Name the blood parasite species.
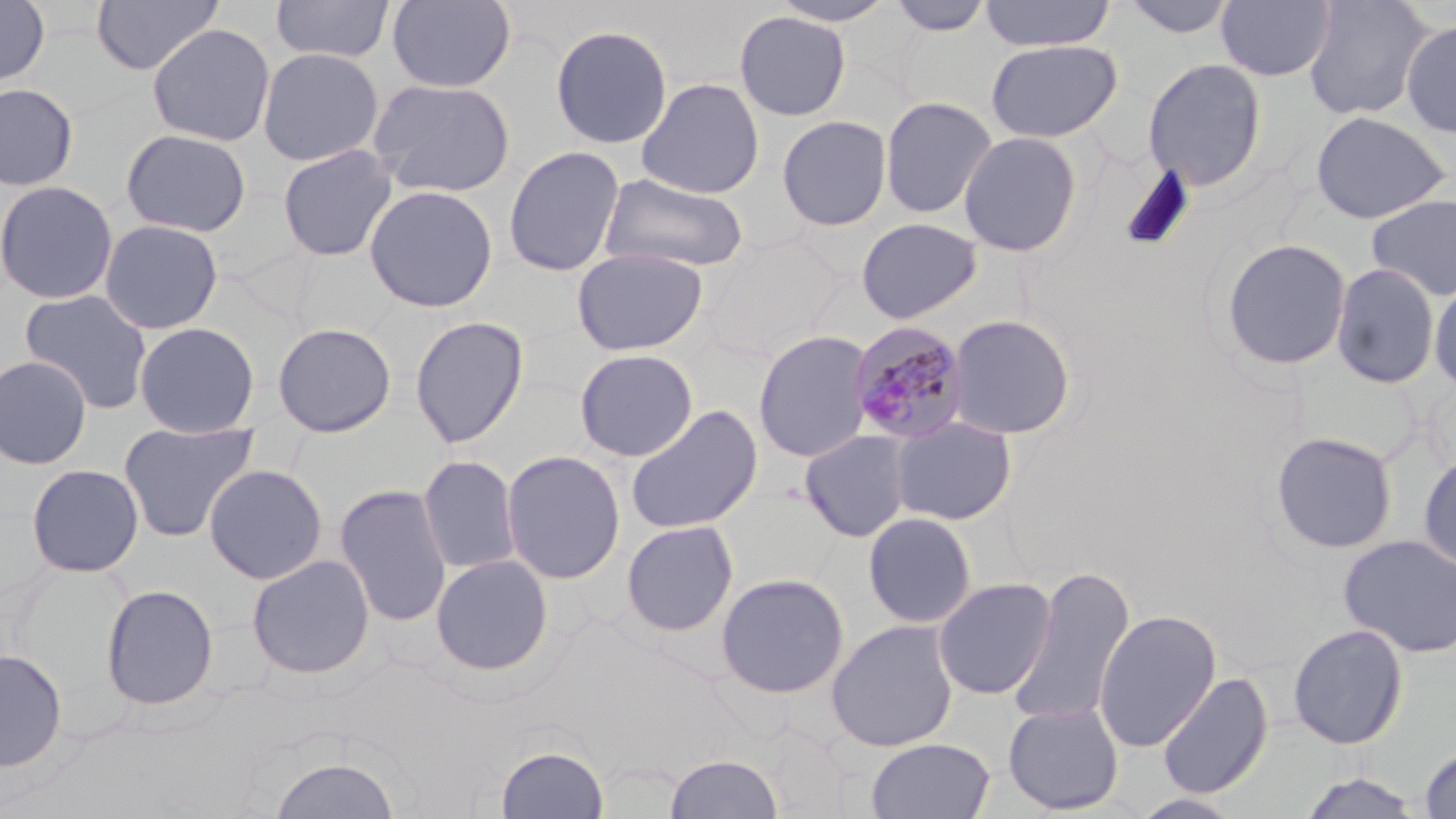
Plasmodium malariae.

Approximate bounding boxes as named x1/y1/x2/y2 corners in pixels. Uninfected red blood cell locations: (x1=0, y1=0, x2=50, y2=88), (x1=90, y1=0, x2=222, y2=76), (x1=270, y1=0, x2=396, y2=64), (x1=387, y1=0, x2=516, y2=93), (x1=769, y1=0, x2=899, y2=26), (x1=886, y1=0, x2=995, y2=36), (x1=980, y1=0, x2=1115, y2=52), (x1=1119, y1=0, x2=1239, y2=39), (x1=1216, y1=0, x2=1336, y2=81), (x1=1302, y1=0, x2=1433, y2=120), (x1=734, y1=10, x2=851, y2=121), (x1=1400, y1=18, x2=1456, y2=140), (x1=147, y1=22, x2=276, y2=146), (x1=550, y1=24, x2=673, y2=149), (x1=985, y1=39, x2=1123, y2=142), (x1=257, y1=46, x2=385, y2=167), (x1=1141, y1=58, x2=1267, y2=190), (x1=367, y1=77, x2=515, y2=198), (x1=636, y1=77, x2=765, y2=199), (x1=0, y1=82, x2=79, y2=192), (x1=879, y1=96, x2=998, y2=219), (x1=1309, y1=110, x2=1451, y2=224), (x1=777, y1=114, x2=892, y2=231), (x1=120, y1=128, x2=252, y2=237), (x1=958, y1=131, x2=1083, y2=257), (x1=276, y1=144, x2=398, y2=262), (x1=503, y1=145, x2=625, y2=276), (x1=598, y1=172, x2=750, y2=273), (x1=0, y1=179, x2=119, y2=305), (x1=363, y1=184, x2=499, y2=312), (x1=1365, y1=194, x2=1456, y2=302), (x1=856, y1=217, x2=983, y2=325), (x1=99, y1=219, x2=223, y2=334), (x1=703, y1=234, x2=843, y2=358), (x1=1218, y1=238, x2=1353, y2=372), (x1=570, y1=246, x2=709, y2=356), (x1=1330, y1=262, x2=1441, y2=389), (x1=1429, y1=279, x2=1456, y2=396), (x1=19, y1=289, x2=154, y2=415), (x1=946, y1=314, x2=1077, y2=440), (x1=409, y1=315, x2=529, y2=449), (x1=134, y1=321, x2=260, y2=437), (x1=271, y1=321, x2=397, y2=438), (x1=752, y1=330, x2=875, y2=463), (x1=574, y1=348, x2=698, y2=462), (x1=0, y1=354, x2=93, y2=469), (x1=625, y1=404, x2=763, y2=534), (x1=889, y1=415, x2=1018, y2=526), (x1=117, y1=420, x2=260, y2=543), (x1=799, y1=429, x2=915, y2=543), (x1=1270, y1=431, x2=1399, y2=555), (x1=501, y1=450, x2=626, y2=584), (x1=1418, y1=451, x2=1456, y2=574), (x1=418, y1=454, x2=521, y2=576), (x1=25, y1=463, x2=145, y2=578), (x1=204, y1=463, x2=328, y2=584), (x1=334, y1=484, x2=452, y2=626), (x1=862, y1=512, x2=977, y2=629), (x1=621, y1=520, x2=739, y2=636), (x1=1339, y1=534, x2=1456, y2=658), (x1=246, y1=553, x2=376, y2=680), (x1=430, y1=554, x2=554, y2=675), (x1=1009, y1=570, x2=1135, y2=727), (x1=715, y1=572, x2=850, y2=699), (x1=933, y1=577, x2=1057, y2=700), (x1=100, y1=583, x2=219, y2=710), (x1=1094, y1=609, x2=1221, y2=751), (x1=825, y1=619, x2=959, y2=752), (x1=1287, y1=623, x2=1409, y2=749), (x1=0, y1=648, x2=67, y2=772), (x1=1156, y1=672, x2=1273, y2=799), (x1=1002, y1=701, x2=1125, y2=815), (x1=866, y1=737, x2=995, y2=819), (x1=495, y1=744, x2=609, y2=819), (x1=1419, y1=746, x2=1456, y2=818), (x1=664, y1=753, x2=784, y2=819), (x1=269, y1=755, x2=400, y2=819), (x1=1296, y1=771, x2=1425, y2=818). Plasmodium malariae-infected red blood cell locations: (x1=847, y1=321, x2=972, y2=444). 1000x magnification. Light microscopy. Image is 1456×819 pixels. Single field of view. May-Grünwald-Giemsa-stained preparation. Thin blood smear.